Identify the cell.
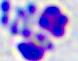

A leukocyte.

modality = photomicrograph
magnification = 400x